Point out each Plasmodium parasite.
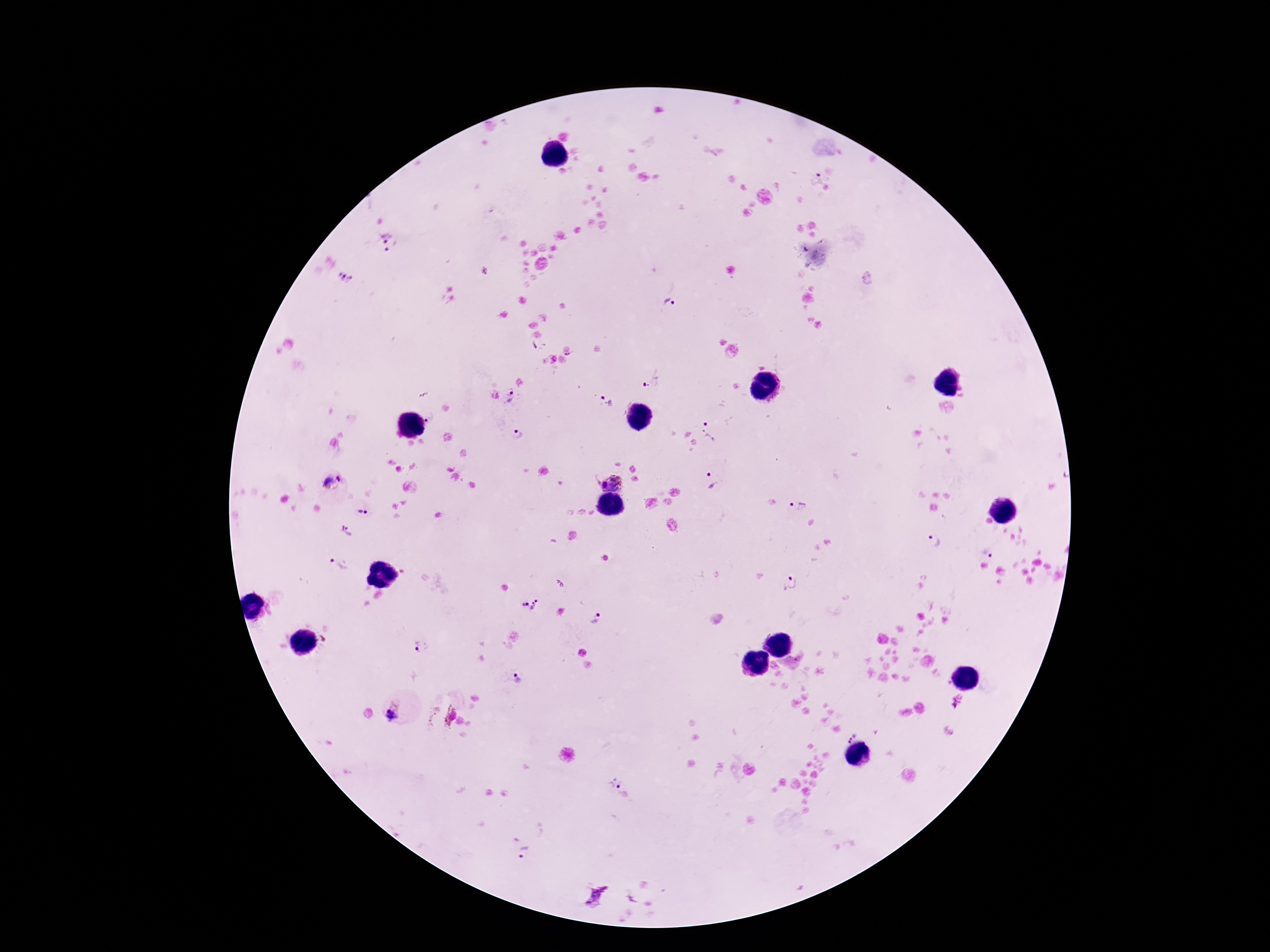
Approximate centers as {x, y} in pixels.
Plasmodium parasites: {818, 178}, {389, 244}, {868, 278}, {344, 279}, {669, 303}, {570, 354}, {652, 379}, {512, 396}, {605, 401}, {432, 418}, {711, 430}, {518, 436}, {714, 482}, {332, 483}, {611, 484}, {798, 507}, {361, 511}, {349, 533}, {934, 541}, {987, 550}, {337, 564}, {792, 583}, {530, 606}, {595, 618}, {421, 649}, {516, 678}, {957, 700}, {399, 711}, {441, 717}, {850, 737}, {614, 781}, {524, 851}, {595, 896}.

{
  "image_size": "1270×952 pixels",
  "capture": "smartphone camera through the microscope eyepiece",
  "field_of_view": "one from this slide",
  "stain": "Giemsa",
  "preparation": "thick peripheral-blood smear",
  "magnification": "100x",
  "patient_malaria_status": "infected"
}